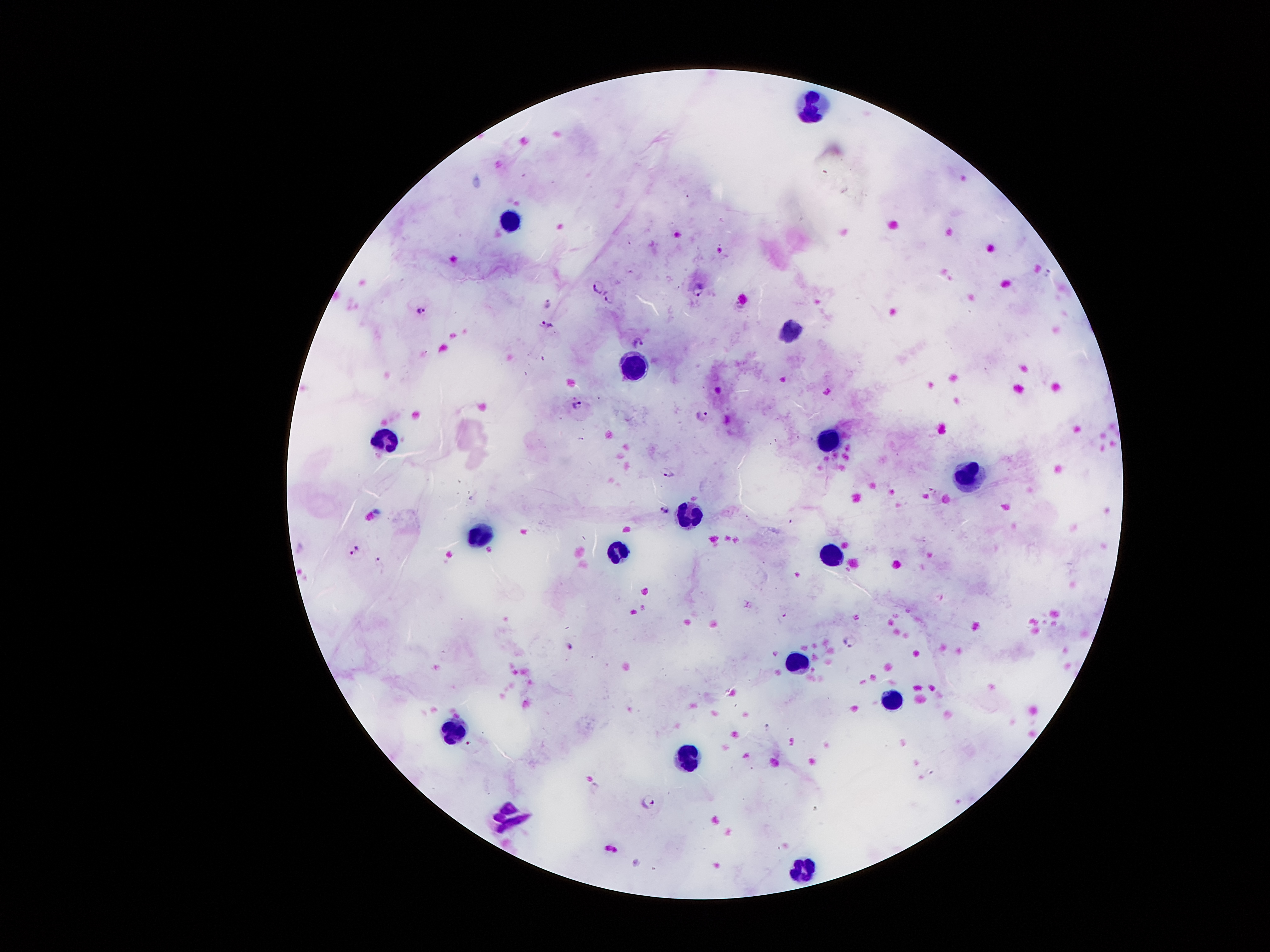

Approximate centers as [x, y] in pixels.
Summary:
  - Plasmodium parasite locations: [597, 286], [697, 288], [606, 299], [547, 305], [423, 308], [546, 322], [637, 342], [577, 404], [702, 414], [666, 471], [665, 511], [355, 550], [851, 642], [570, 645], [649, 800]
  - Leukocyte locations: [810, 105], [510, 219], [782, 333], [635, 369], [386, 442], [822, 442], [969, 474], [690, 514], [477, 534], [621, 553], [830, 556], [794, 664], [893, 694], [447, 732], [690, 753], [511, 813], [802, 864]
  - Magnification: 100x
  - Patient malaria status: infected with Plasmodium falciparum
  - Capture: smartphone camera through the microscope eyepiece
  - Image size: 1270×952 pixels
  - Stain: Giemsa
  - Preparation: thick blood film
  - Field of view: one from this slide